Comment on the morphology of the erythrocytes.
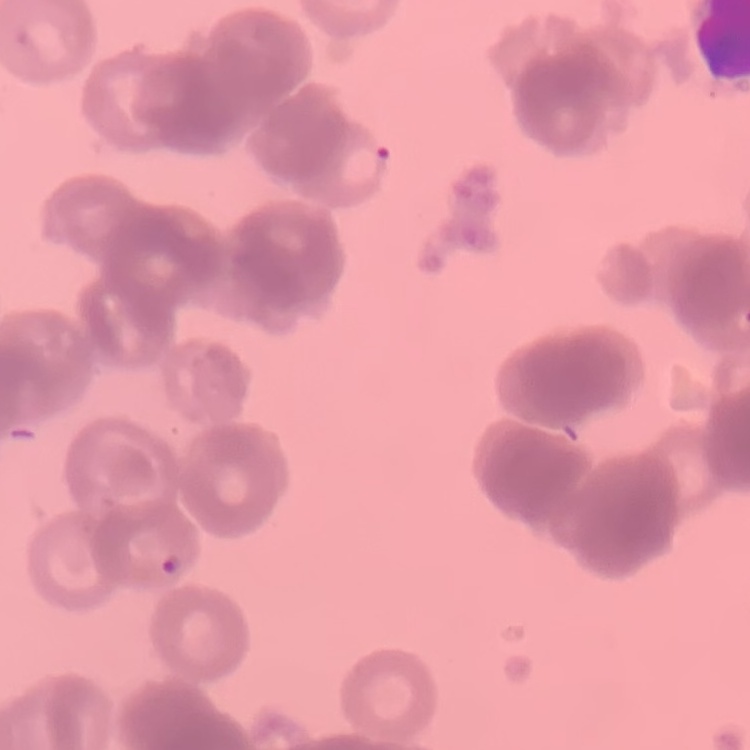
They show rouleaux formation.

Square crop of a larger photomicrograph. Thin peripheral smear. Field's or Giemsa stain.